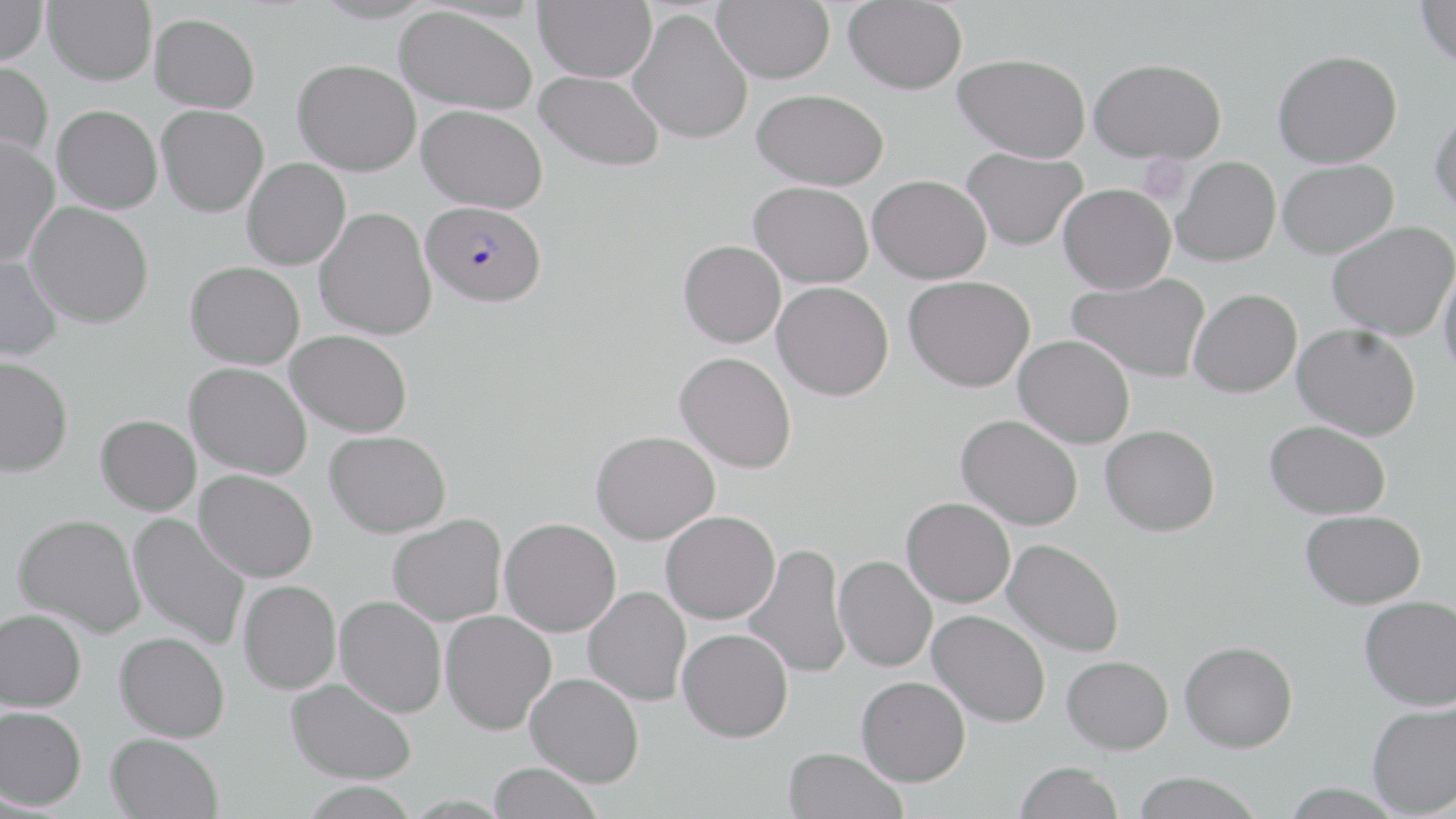

Approximate bounding boxes as (x1, y1, x2, y2) in pixels. Platelet locations: (1138, 154, 1192, 205). Plasmodium falciparum-infected red blood cell locations: (422, 199, 547, 307). Uninfected red blood cell locations: (0, 0, 47, 65), (43, 0, 156, 85), (534, 0, 656, 81), (713, 0, 834, 83), (843, 0, 967, 93), (1414, 0, 1456, 69), (395, 5, 537, 114), (627, 8, 754, 145), (149, 12, 260, 112), (1273, 49, 1403, 168), (955, 52, 1091, 162), (1089, 57, 1227, 163), (293, 59, 421, 175), (0, 60, 53, 165), (536, 70, 664, 171), (751, 88, 888, 189), (53, 104, 163, 214), (157, 104, 269, 216), (417, 104, 547, 213), (1430, 105, 1456, 221), (0, 135, 60, 267), (962, 147, 1088, 251), (1172, 156, 1281, 266), (242, 158, 350, 269), (1278, 159, 1399, 259), (868, 174, 992, 283), (749, 181, 874, 287), (1059, 183, 1176, 294), (25, 202, 154, 328), (314, 207, 437, 340), (1327, 220, 1455, 340), (678, 239, 786, 347), (0, 252, 62, 362), (1438, 258, 1456, 381), (186, 261, 305, 369), (1067, 273, 1211, 382), (904, 275, 1036, 391), (773, 282, 894, 400), (1189, 288, 1302, 398), (1292, 323, 1421, 440), (286, 329, 413, 437), (1014, 335, 1135, 448), (675, 351, 797, 473), (0, 355, 73, 477), (185, 362, 312, 480), (96, 414, 201, 515), (957, 414, 1083, 530), (1264, 420, 1391, 519), (1100, 425, 1220, 536), (325, 430, 451, 538), (590, 430, 720, 544), (194, 469, 318, 582), (902, 497, 1015, 607), (1300, 509, 1426, 609), (662, 510, 780, 624), (128, 512, 250, 650), (14, 513, 145, 637), (388, 513, 507, 626), (499, 517, 621, 636), (1002, 539, 1124, 657), (743, 543, 850, 679), (834, 556, 937, 671), (239, 580, 342, 694), (583, 586, 691, 706), (1359, 594, 1456, 710), (335, 595, 447, 717), (0, 608, 86, 710), (440, 610, 556, 735), (928, 610, 1050, 727), (677, 628, 793, 742), (115, 631, 230, 741), (1180, 640, 1298, 752), (1062, 655, 1173, 754), (525, 673, 644, 787), (856, 676, 970, 786), (286, 677, 416, 784), (1366, 701, 1456, 817), (0, 706, 87, 809), (106, 732, 224, 819), (783, 747, 907, 819), (1015, 761, 1123, 819), (489, 762, 602, 819), (1131, 771, 1263, 819), (300, 781, 419, 819). Slide-level diagnosis: Plasmodium falciparum. May-Grünwald-Giemsa stain. Image is 1456×819 pixels. Thin blood smear. Light microscopy. 1000x magnification. Single field of view.